Locate every malaria parasite.
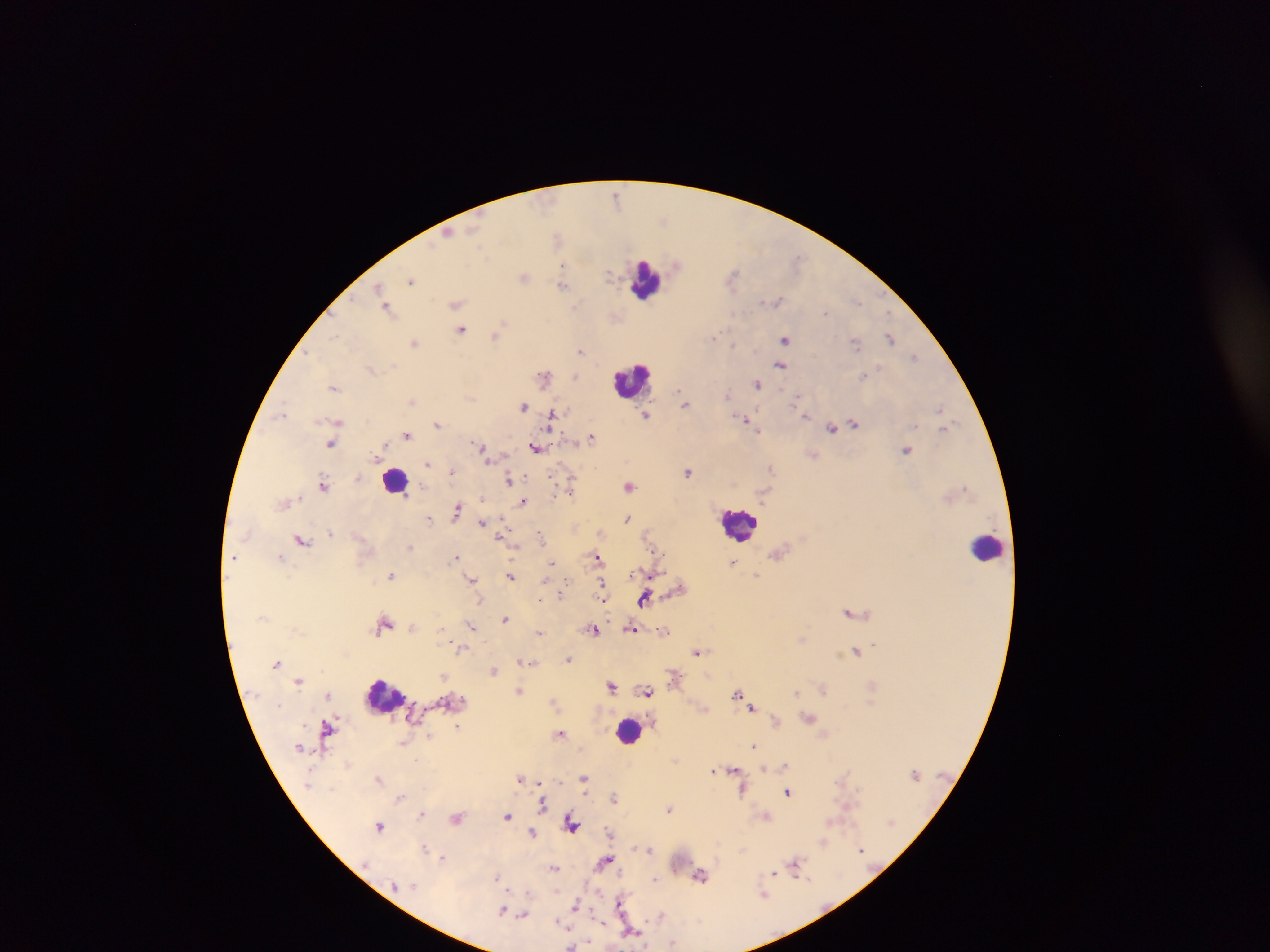
Approximate centers as [x, y] in pixels.
Malaria parasites: [618, 197], [557, 237], [677, 264], [563, 265], [610, 274], [732, 276], [524, 277], [412, 280], [563, 285], [378, 287], [383, 297], [777, 300], [858, 302], [456, 303], [576, 305], [386, 307], [826, 312], [503, 323], [461, 331], [334, 336], [495, 336], [714, 336], [785, 338], [890, 338], [414, 342], [855, 344], [580, 350], [309, 353], [914, 356], [780, 365], [864, 375], [574, 376], [544, 377], [757, 384], [334, 388], [680, 393], [729, 395], [683, 398], [796, 398], [411, 401], [685, 404], [522, 406], [939, 408], [802, 412], [283, 413], [646, 415], [805, 415], [552, 416], [746, 419], [339, 421], [437, 423], [854, 424], [946, 427], [756, 428], [832, 428], [407, 435], [592, 437], [331, 445], [482, 448], [536, 449], [906, 450], [814, 455], [429, 463], [771, 468], [451, 472], [688, 472], [509, 479], [324, 486], [571, 486], [629, 487], [523, 502], [457, 510], [429, 518], [627, 519], [482, 523], [330, 533], [539, 534], [301, 539], [410, 546], [597, 556], [234, 557], [280, 557], [456, 557], [553, 563], [732, 563], [390, 575], [757, 575], [510, 576], [473, 579], [601, 585], [644, 598], [850, 612], [505, 619], [385, 623], [472, 627], [632, 629], [594, 631], [664, 631], [539, 632], [460, 648], [855, 651], [697, 652], [568, 660], [276, 663], [493, 670], [444, 677], [299, 680], [612, 686], [824, 689], [520, 690], [648, 691], [796, 692], [738, 693], [327, 695], [554, 701], [752, 707], [809, 718], [776, 721], [458, 726], [326, 729], [560, 733], [753, 746], [415, 760], [785, 764], [763, 768], [733, 770], [713, 771], [520, 778], [584, 778], [379, 779], [540, 783], [742, 791], [788, 792], [614, 796], [400, 797], [542, 804], [670, 809], [422, 813], [507, 816], [766, 816], [457, 819], [571, 823], [379, 826], [609, 831], [533, 832], [823, 843], [425, 848], [650, 850], [862, 850], [442, 857], [605, 860], [795, 864], [554, 868], [774, 874], [700, 876], [497, 877], [655, 879], [764, 894], [620, 901], [576, 904], [503, 910], [661, 915], [523, 916], [560, 923], [632, 931], [673, 943], [571, 946].

capture = mobile-phone photograph through a microscope
field of view = single
image size = 1270×952 pixels
preparation = thick blood smear
leukocyte locations = approximate centers as [x, y] in pixels: [645, 281], [630, 380], [394, 480], [739, 524], [988, 547], [383, 696], [628, 730]
country = Ghana